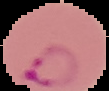
Cell region segmented out of the field of view; the surrounding area is masked to black. From a thin blood film. Malaria status: parasitized. Image is 109×91 pixels.